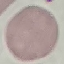
Malaria status: uninfected. Acquired by smartphone through the microscope eyepiece. Giemsa-stained preparation. Cell patch, automatically extracted from a larger field of view and resized to 64 × 64 pixels. Thin blood film.